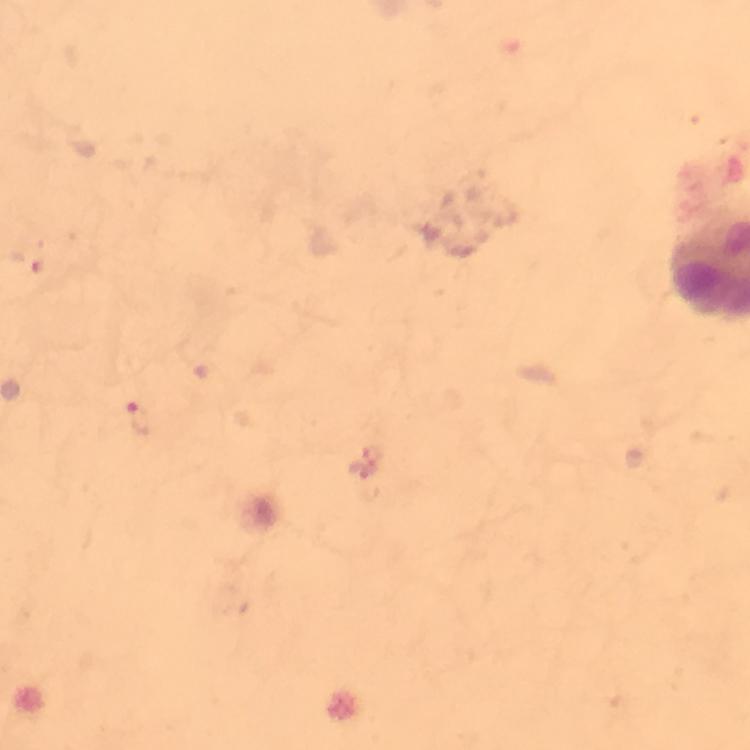
Approximate centers as {x, y} in pixels.
Summary:
  - Plasmodium parasite locations: {142, 419}
  - Context: from a diagnostic examination for malaria
  - Stain: Giemsa
  - Cropped from: a single field of view
  - Image size: 750×750 pixels
  - Capture: smartphone camera through the microscope
  - Immersion oil: applied
  - Preparation: thick blood film
  - Magnification: 100x